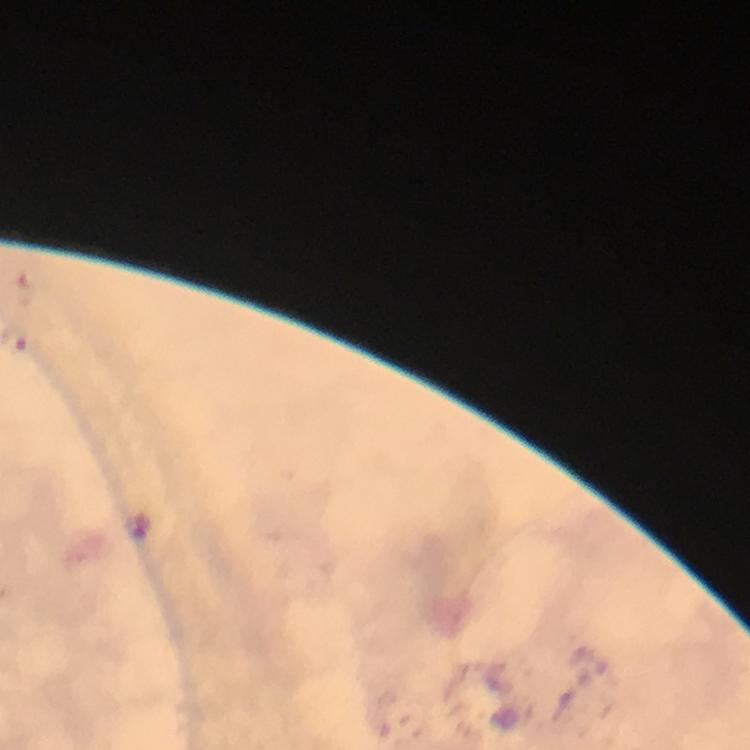
{
  "capture": "smartphone mounted on the microscope",
  "stain": "Giemsa",
  "cropped_from": "a single field of view",
  "plasmodium_parasite_locations": "approximate centers as {x, y} in pixels: {138, 524}",
  "immersion_oil": "used",
  "context": "from a diagnostic examination for malaria",
  "magnification": "100x",
  "image_size": "750×750 pixels",
  "preparation": "thick blood film"
}